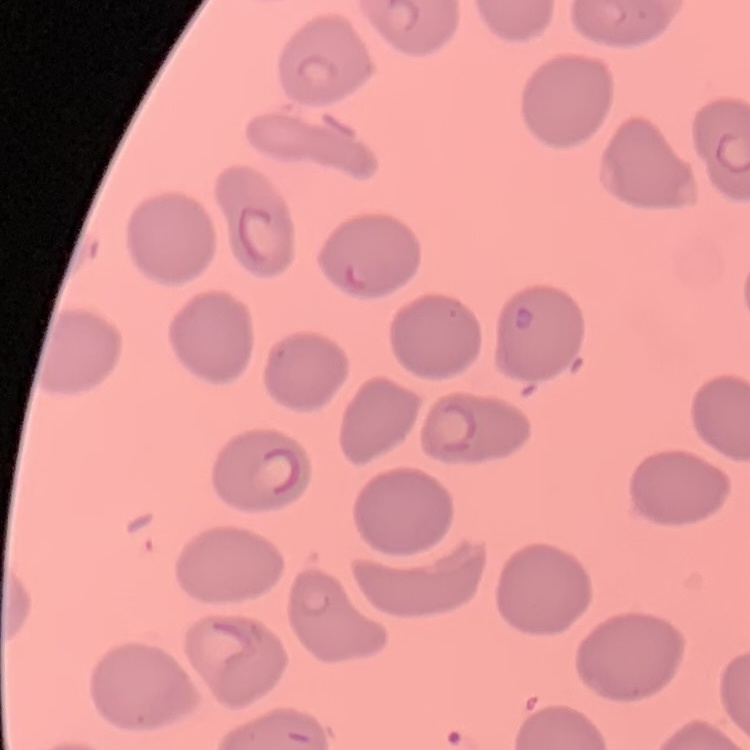
red blood cell morphology = no rouleaux formation
stain = Field's or Giemsa
preparation = thin peripheral smear
image type = square crop of a larger photomicrograph